Point out each leukocyte.
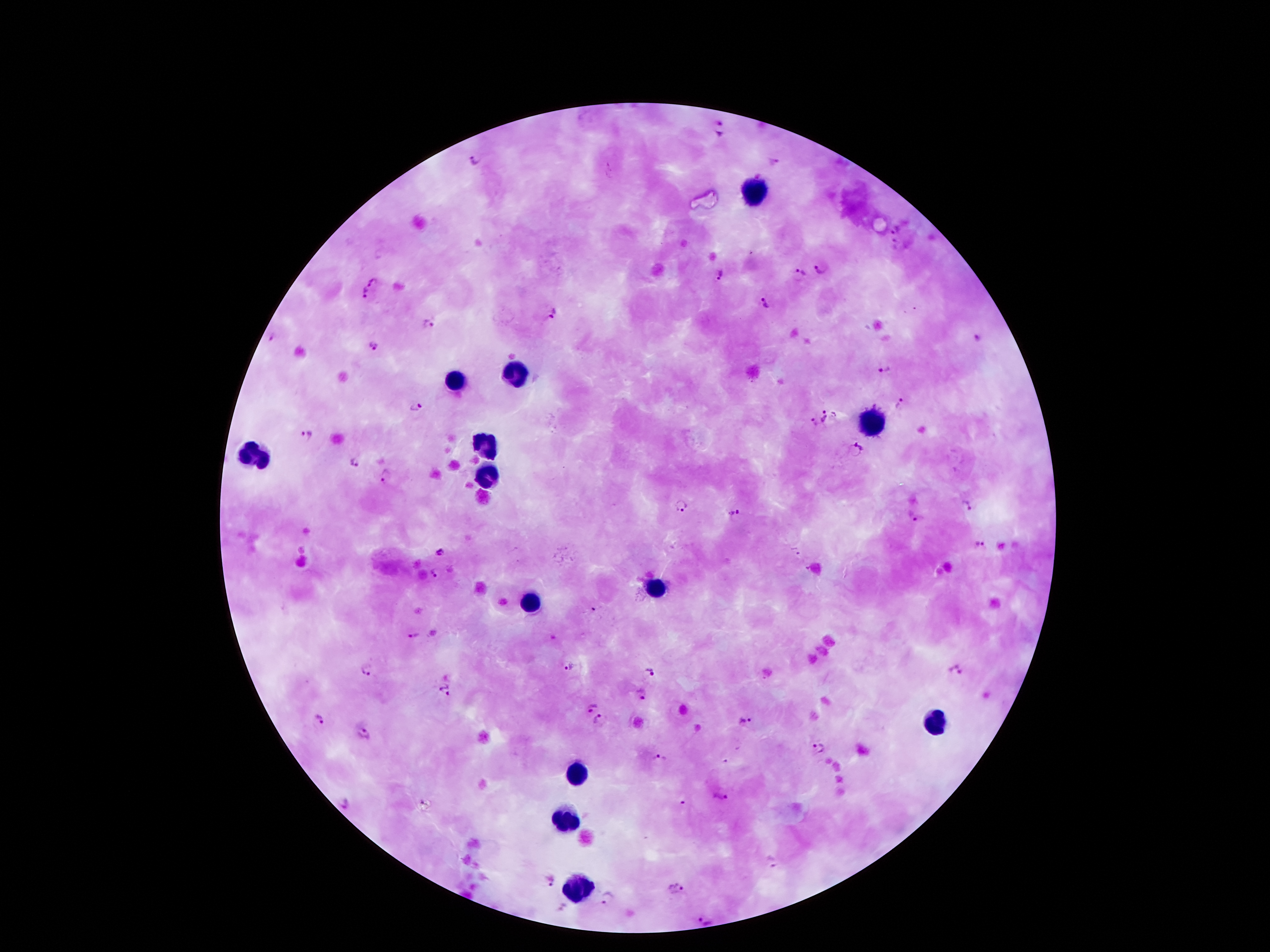
Approximate centers as {x, y} in pixels.
Leukocytes: {755, 191}, {514, 375}, {454, 381}, {870, 426}, {485, 443}, {257, 454}, {485, 474}, {655, 587}, {527, 602}, {934, 722}, {578, 773}, {564, 821}, {582, 886}.

Malaria parasite locations: {720, 129}, {475, 159}, {894, 230}, {893, 242}, {821, 268}, {801, 273}, {719, 275}, {371, 283}, {363, 293}, {765, 303}, {552, 313}, {427, 324}, {977, 338}, {270, 340}, {373, 347}, {884, 370}, {898, 402}, {415, 407}, {835, 413}, {825, 415}, {813, 422}, {307, 435}, {855, 448}, {357, 463}, {385, 476}, {680, 505}, {967, 507}, {733, 512}, {913, 515}, {980, 545}, {797, 551}, {439, 552}, {436, 572}, {595, 606}, {412, 636}, {570, 665}, {365, 668}, {650, 669}, {954, 669}, {445, 689}, {641, 694}, {590, 705}, {318, 719}, {599, 719}, {748, 721}, {364, 734}, {818, 748}, {661, 757}, {721, 797}, {343, 801}, {772, 861}, {548, 878}, {677, 889}, {608, 899}, {707, 921}. Smartphone photograph taken through the microscope eyepiece. Image is 1270×952 pixels. 100x magnification. One field from this slide. Patient malaria status: positive for Plasmodium falciparum. Giemsa stain. Thick peripheral-blood smear.